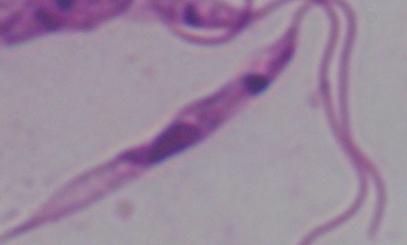

Micrograph. A Leishmania parasite is shown. Captured at 1000x magnification.